Locate the cells, classifying each as a parasitized RBC, an uninfected RBC, or a WBC.
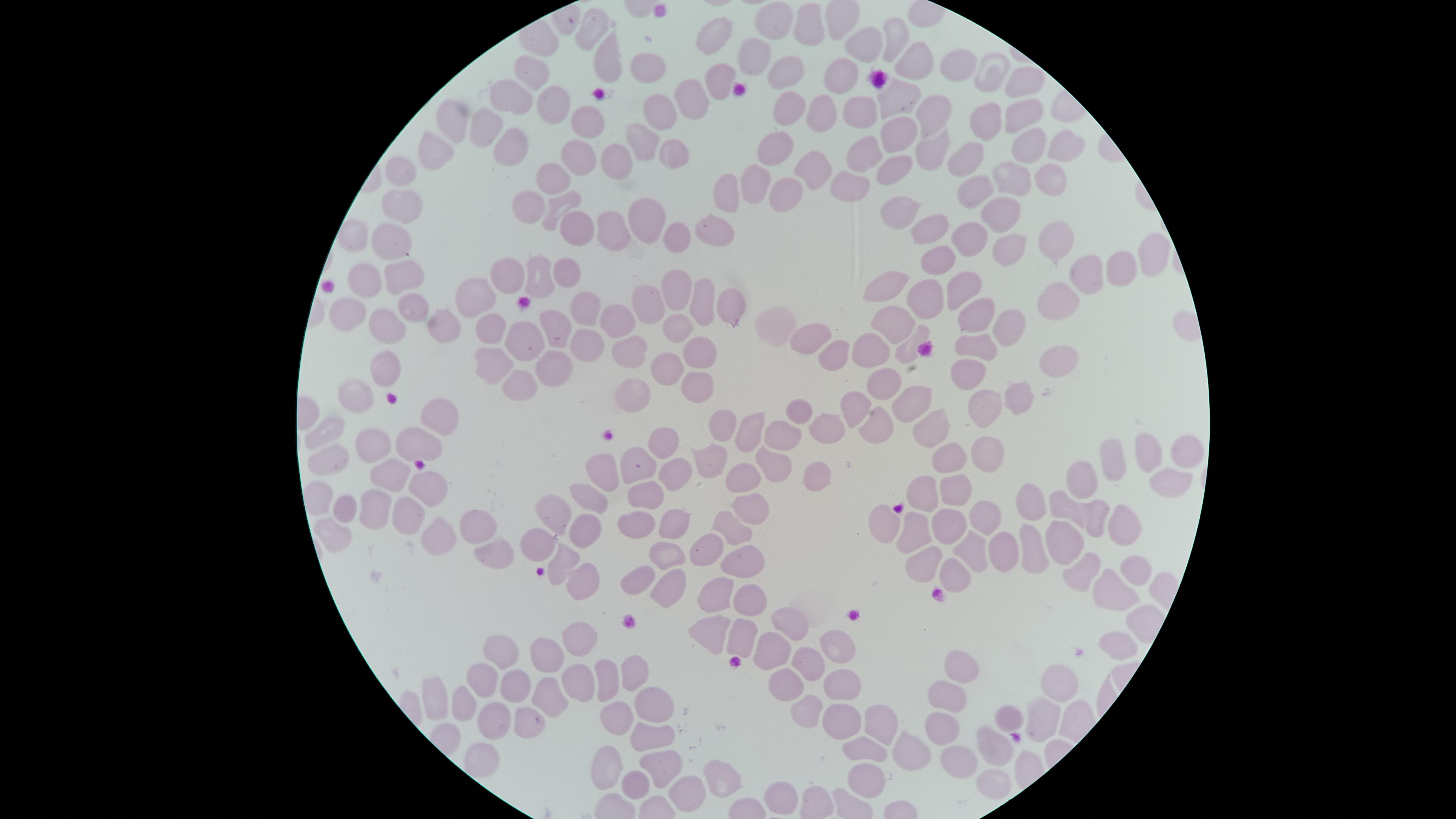
No parasitized RBCs identified.
Approximate marker points, in pixels from the top-left corner.
Uninfected RBCs: (x=778, y=17), (x=594, y=20), (x=807, y=25), (x=719, y=32), (x=894, y=36), (x=867, y=42), (x=751, y=57), (x=603, y=60), (x=918, y=62), (x=652, y=64), (x=961, y=64), (x=990, y=70), (x=788, y=71), (x=536, y=72), (x=725, y=77), (x=835, y=77), (x=1028, y=80), (x=514, y=95), (x=900, y=98), (x=687, y=101), (x=554, y=106), (x=932, y=106), (x=658, y=108), (x=788, y=110), (x=860, y=110), (x=823, y=112), (x=455, y=116), (x=1026, y=117), (x=586, y=120), (x=989, y=125), (x=483, y=126), (x=898, y=127), (x=644, y=138), (x=1030, y=142), (x=510, y=144), (x=772, y=145), (x=929, y=146), (x=869, y=147), (x=1066, y=148), (x=671, y=149), (x=432, y=153), (x=974, y=155), (x=624, y=159), (x=573, y=161), (x=894, y=167), (x=399, y=169), (x=812, y=170), (x=1011, y=178), (x=543, y=182), (x=1046, y=182), (x=757, y=186), (x=723, y=187), (x=853, y=189), (x=982, y=189), (x=786, y=192), (x=556, y=202), (x=1000, y=204), (x=400, y=206), (x=519, y=206), (x=901, y=208), (x=647, y=216), (x=934, y=221), (x=580, y=222), (x=615, y=228), (x=967, y=231), (x=716, y=232), (x=670, y=237), (x=388, y=244), (x=1053, y=244), (x=1014, y=250), (x=1155, y=258), (x=939, y=259), (x=398, y=266), (x=1121, y=268), (x=1090, y=271), (x=368, y=272), (x=567, y=272), (x=536, y=275), (x=891, y=276), (x=511, y=279), (x=962, y=284), (x=674, y=285), (x=476, y=293), (x=1055, y=294), (x=920, y=299), (x=411, y=301), (x=701, y=301), (x=727, y=304), (x=652, y=306), (x=340, y=307), (x=586, y=309), (x=976, y=317), (x=617, y=318), (x=1006, y=318), (x=443, y=319), (x=899, y=321), (x=394, y=323), (x=491, y=323), (x=772, y=324), (x=678, y=329), (x=554, y=330), (x=806, y=334), (x=588, y=335), (x=525, y=339), (x=976, y=341), (x=871, y=345), (x=911, y=346), (x=634, y=347), (x=839, y=350), (x=700, y=351), (x=1057, y=357), (x=491, y=359), (x=671, y=364), (x=552, y=365), (x=964, y=370), (x=388, y=373), (x=520, y=376), (x=688, y=383), (x=884, y=383), (x=635, y=387), (x=1021, y=395), (x=357, y=397), (x=910, y=398), (x=985, y=404), (x=856, y=406), (x=797, y=410), (x=440, y=417), (x=724, y=422), (x=827, y=425), (x=877, y=426), (x=933, y=426), (x=749, y=430), (x=326, y=431), (x=781, y=434), (x=418, y=440), (x=372, y=441), (x=664, y=442), (x=993, y=448), (x=1156, y=450), (x=1189, y=450), (x=1115, y=456), (x=775, y=458), (x=333, y=459), (x=708, y=459), (x=646, y=461), (x=946, y=461), (x=675, y=466), (x=601, y=469), (x=814, y=472), (x=394, y=473), (x=745, y=474), (x=1089, y=477), (x=1166, y=481), (x=428, y=486), (x=644, y=490), (x=949, y=491), (x=921, y=492), (x=318, y=494), (x=590, y=498), (x=1041, y=498), (x=1068, y=503), (x=751, y=508), (x=344, y=509), (x=372, y=509), (x=554, y=510), (x=410, y=513), (x=986, y=515), (x=1098, y=515), (x=943, y=519), (x=890, y=520), (x=476, y=521), (x=634, y=521), (x=1117, y=521), (x=681, y=524), (x=590, y=526), (x=731, y=527), (x=911, y=531), (x=436, y=533), (x=333, y=534), (x=1064, y=536), (x=537, y=540), (x=709, y=544), (x=975, y=544), (x=1038, y=544), (x=496, y=545), (x=1010, y=549), (x=664, y=552), (x=563, y=556), (x=743, y=556), (x=919, y=569), (x=960, y=572), (x=1136, y=572), (x=1087, y=573), (x=633, y=575), (x=579, y=582), (x=667, y=583), (x=1112, y=588), (x=715, y=593), (x=748, y=596), (x=797, y=622), (x=715, y=634), (x=739, y=635), (x=581, y=639), (x=839, y=646), (x=505, y=648), (x=1118, y=648), (x=771, y=649), (x=546, y=655), (x=633, y=663), (x=807, y=663), (x=962, y=665), (x=478, y=678), (x=608, y=679), (x=577, y=680), (x=840, y=681), (x=522, y=684), (x=1051, y=685), (x=785, y=688), (x=549, y=697), (x=440, y=699), (x=946, y=699), (x=466, y=703), (x=656, y=706), (x=810, y=710), (x=1011, y=715), (x=840, y=716), (x=494, y=717), (x=619, y=718), (x=1041, y=718), (x=523, y=719), (x=876, y=719), (x=934, y=731), (x=648, y=734), (x=994, y=742), (x=866, y=744), (x=480, y=756), (x=910, y=757), (x=956, y=760), (x=612, y=765), (x=659, y=767), (x=860, y=773), (x=988, y=779), (x=717, y=780), (x=639, y=783), (x=685, y=789), (x=781, y=792).
No WBCs identified.

Image is 1456×819 pixels. Giemsa-stained preparation. Smartphone photograph through the microscope eyepiece. Circular visible region. Single field of view. Thin smear of blood.